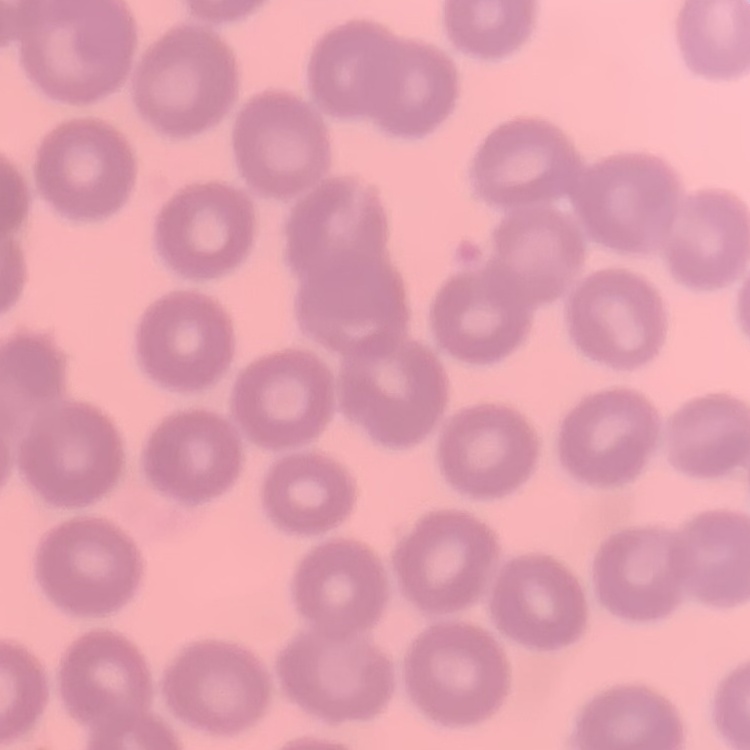

Summary:
  - Red blood cell morphology: no rouleaux formation
  - Image type: square crop of a larger photomicrograph
  - Stain: Field's or Giemsa
  - Preparation: thin peripheral smear